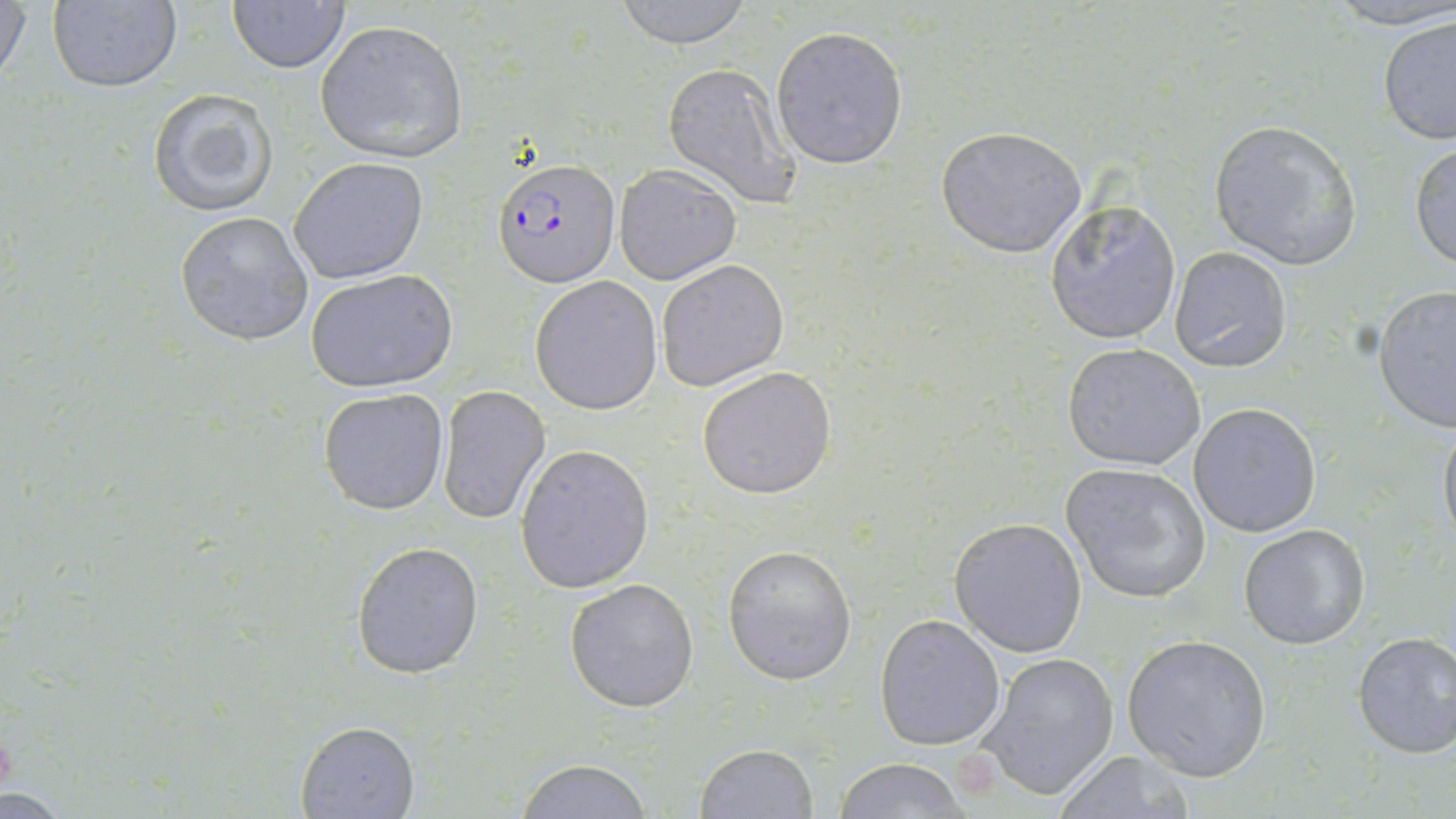

Summary:
  - Coordinate format: approximate bounding boxes as (x1,y1)-(x2,y2) corner pairs in pixels
  - Uninfected red blood cell locations: (1,0)-(31,92), (45,0)-(184,92), (226,0)-(350,72), (609,0)-(758,48), (1323,0)-(1456,30), (1377,13)-(1456,145), (314,20)-(468,162), (772,26)-(908,169), (662,61)-(801,207), (145,88)-(279,216), (1208,119)-(1362,271), (936,126)-(1087,258), (1410,140)-(1456,271), (288,156)-(429,285), (614,166)-(742,285), (1045,200)-(1182,345), (174,211)-(314,346), (1169,247)-(1291,372), (657,258)-(789,392), (304,269)-(459,393), (530,276)-(662,414), (1374,286)-(1456,433), (1062,342)-(1206,470), (697,366)-(838,501), (436,384)-(551,525), (319,388)-(449,514), (1189,402)-(1323,538), (1438,413)-(1456,553), (515,445)-(653,593), (1061,461)-(1212,603), (949,517)-(1090,656), (1238,523)-(1371,649), (352,542)-(484,678), (722,544)-(857,685), (564,577)-(699,712), (874,613)-(1006,749), (1351,631)-(1456,758), (1121,633)-(1272,782), (975,652)-(1119,801), (293,719)-(421,819), (695,744)-(819,818), (1053,750)-(1196,818), (834,758)-(970,818), (514,759)-(653,817)
  - Plasmodium falciparum-infected red blood cell locations: (493,159)-(620,285)
  - Slide-level diagnosis: Plasmodium falciparum
  - Stain: May-Grünwald-Giemsa
  - Modality: light microscopy
  - Magnification: 1000x
  - Field of view: one of a larger specimen
  - Image size: 1456×819 pixels
  - Preparation: thin blood film